Report the malaria status of this cell.
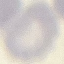
Uninfected.

Giemsa stain. Acquired by smartphone through the microscope eyepiece. Thin blood film. Automatically extracted cell patch, resized to 64 × 64 pixels.